Give the position of every Plasmodium parasite visible.
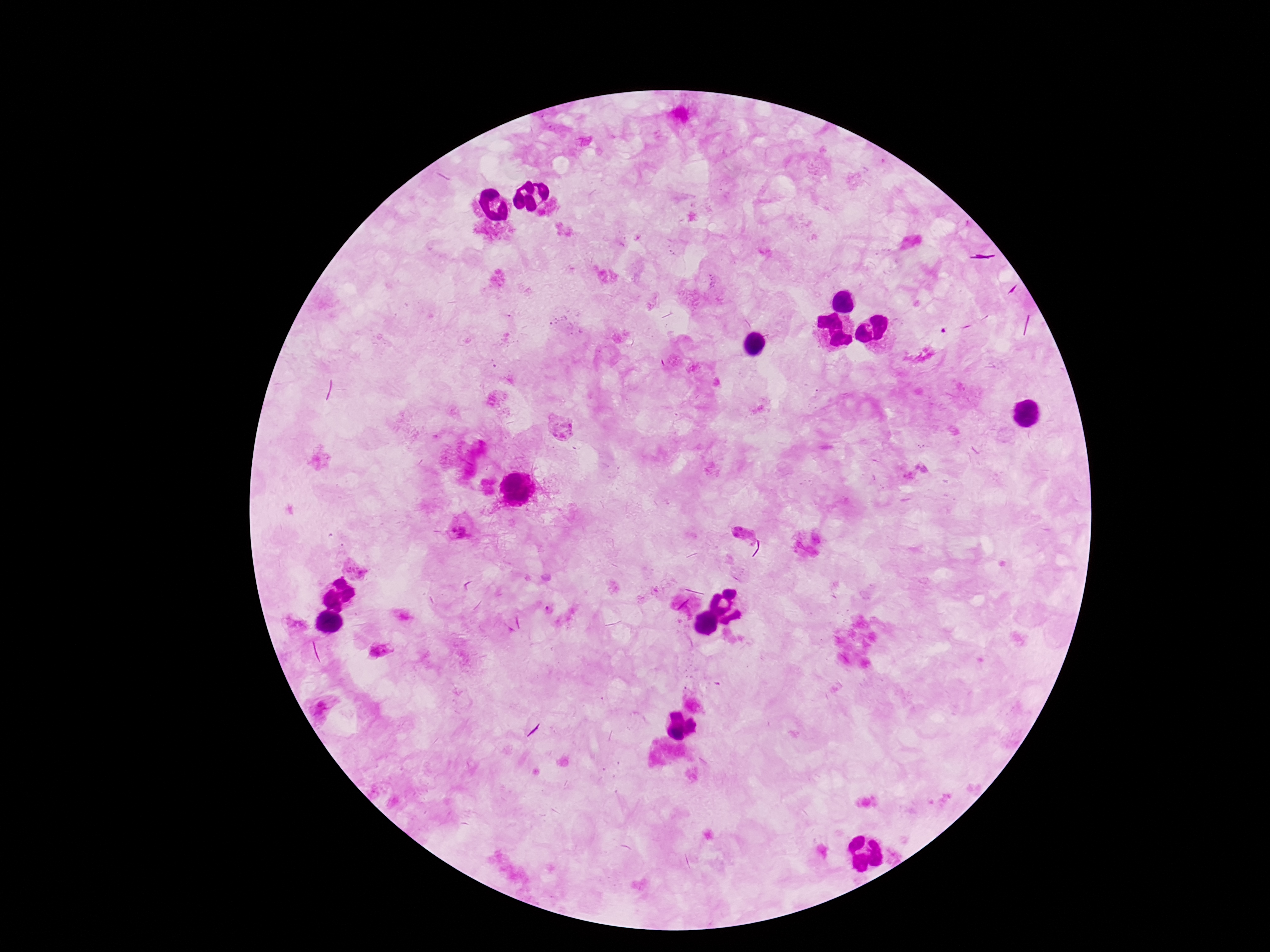
Approximate centers as (x, y) in pixels.
Plasmodium parasites: (560, 427), (916, 472), (462, 527), (745, 536), (357, 568), (549, 609), (295, 622), (380, 651).

Summary:
  - Image size: 1270×952 pixels
  - Stain: Giemsa
  - Field of view: one from this slide
  - Capture: smartphone camera through the microscope eyepiece
  - Preparation: thick blood smear
  - Magnification: 100x
  - Patient malaria status: infected